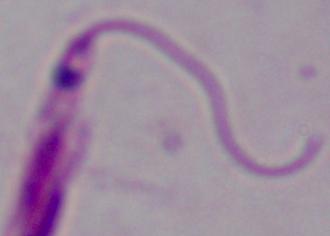
Micrograph. 1000x magnification. A Leishmania parasite is shown.